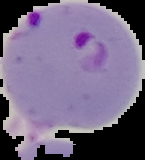

result: malaria parasites detected
image_type: segmented cell region with the area outside set to black
preparation: thin blood film
image_size: 145×160 pixels